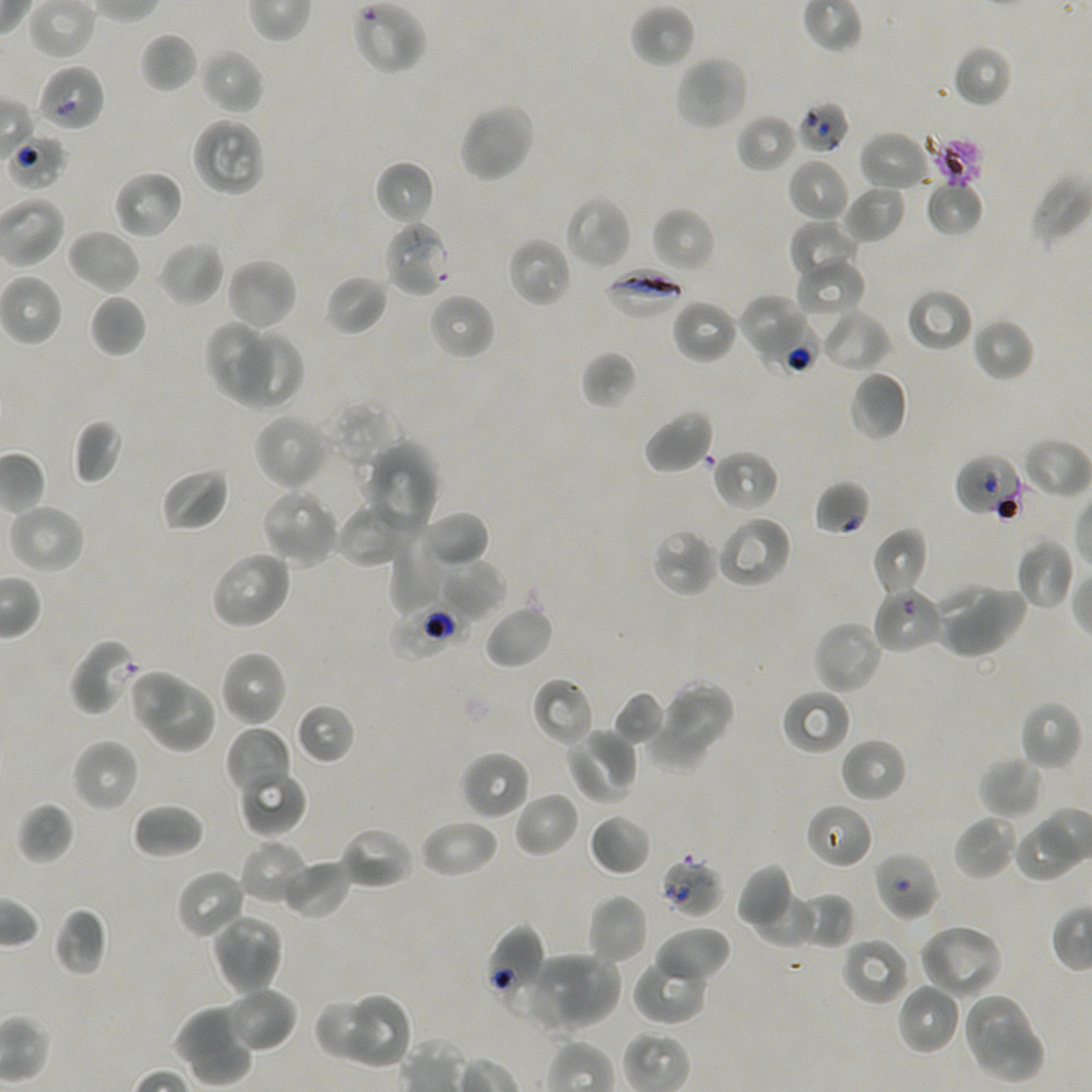

Approximate bounding boxes as {x1, y1, x2, y2} in pixels. Not every red blood cell is marked. Locations of uninfected red blood cells: {353, 0, 427, 75}, {630, 3, 695, 69}, {140, 32, 198, 94}, {952, 43, 1013, 108}, {198, 48, 266, 115}, {674, 54, 750, 132}, {458, 101, 536, 184}, {735, 113, 798, 174}, {190, 117, 266, 198}, {858, 130, 932, 193}, {787, 158, 850, 224}, {375, 160, 436, 225}, {111, 169, 183, 240}, {1030, 174, 1092, 246}, {925, 180, 985, 237}, {840, 182, 906, 244}, {564, 195, 632, 271}, {651, 207, 715, 274}, {788, 219, 861, 287}, {67, 228, 141, 295}, {506, 236, 572, 308}, {158, 240, 225, 307}, {224, 257, 298, 332}, {795, 259, 867, 321}, {324, 274, 388, 335}, {905, 288, 973, 352}, {89, 293, 147, 358}, {427, 293, 495, 360}, {737, 293, 810, 365}, {671, 298, 740, 365}, {818, 308, 892, 374}, {971, 317, 1034, 382}, {204, 321, 274, 402}, {238, 327, 304, 413}, {580, 350, 638, 410}, {848, 371, 909, 441}, {640, 408, 715, 475}, {252, 412, 331, 492}, {73, 418, 123, 486}, {1021, 436, 1090, 500}, {363, 441, 439, 536}, {711, 449, 780, 513}, {160, 467, 229, 532}, {260, 488, 341, 568}, {334, 499, 418, 569}, {7, 502, 86, 575}, {422, 508, 491, 566}, {716, 514, 793, 589}, {871, 527, 928, 598}, {651, 528, 718, 597}, {388, 532, 455, 613}, {1015, 537, 1075, 611}, {208, 549, 293, 631}, {437, 558, 507, 621}, {934, 581, 1005, 655}, {947, 587, 1029, 660}, {481, 604, 553, 669}, {812, 620, 884, 695}, {219, 649, 288, 728}, {130, 668, 188, 735}, {532, 676, 594, 748}, {651, 680, 733, 763}, {149, 684, 217, 758}, {781, 688, 852, 755}, {613, 691, 666, 746}, {1017, 700, 1082, 771}, {295, 703, 355, 765}, {643, 708, 716, 772}, {225, 726, 293, 798}, {564, 727, 640, 807}, {839, 737, 908, 803}, {71, 738, 140, 813}, {460, 750, 530, 820}, {979, 757, 1043, 820}, {238, 768, 308, 837}, {513, 791, 579, 858}, {17, 801, 75, 865}, {131, 803, 204, 859}, {805, 803, 874, 870}, {589, 813, 651, 876}, {953, 814, 1018, 881}, {418, 818, 499, 879}, {1012, 822, 1077, 882}, {338, 824, 416, 890}, {240, 839, 311, 907}, {279, 858, 352, 920}, {735, 862, 795, 932}, {175, 867, 248, 941}, {750, 888, 818, 948}, {797, 891, 856, 949}, {587, 894, 648, 966}, {53, 907, 109, 977}, {212, 913, 283, 975}, {917, 923, 1003, 1000}, {653, 926, 731, 987}, {840, 935, 911, 1006}, {212, 936, 285, 996}, {529, 951, 621, 1033}, {633, 953, 709, 1025}, {896, 982, 962, 1056}, {221, 984, 297, 1054}, {349, 991, 411, 1069}, {961, 991, 1034, 1063}, {313, 997, 382, 1063}, {175, 1005, 254, 1087}, {971, 1019, 1048, 1085}. Locations of infected red blood cells: {382, 219, 451, 297}, {604, 267, 687, 321}. Locations of red blood cells of indeterminate infection status: {37, 64, 106, 132}, {797, 99, 851, 156}, {4, 132, 69, 191}, {750, 313, 818, 378}, {954, 453, 1025, 518}, {814, 480, 871, 536}, {873, 585, 945, 655}, {389, 603, 465, 661}, {68, 638, 141, 717}, {873, 850, 941, 922}, {659, 856, 723, 919}, {486, 925, 547, 1010}. Thin blood smear. Giemsa-stained preparation. Oil immersion, 100x objective (numerical aperture 1.45). Image is 1092×1092 pixels. Donor blood group A+/O+. Single field of view. Plasmodium falciparum strain NF54 in static in-vitro culture.